Classify this cell by malaria status.
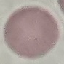

It is uninfected.

stain: Giemsa
capture: smartphone camera at the microscope eyepiece
image_type: automatically extracted cell patch, resized to 64 × 64 pixels
preparation: thin blood smear